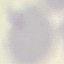
Malaria status: uninfected. Giemsa stain. Cell patch, automatically extracted from a larger field of view and resized to 64 × 64 pixels. Thin blood film. Acquired by smartphone through the microscope eyepiece.